Give the position of every Plasmodium parasite visible.
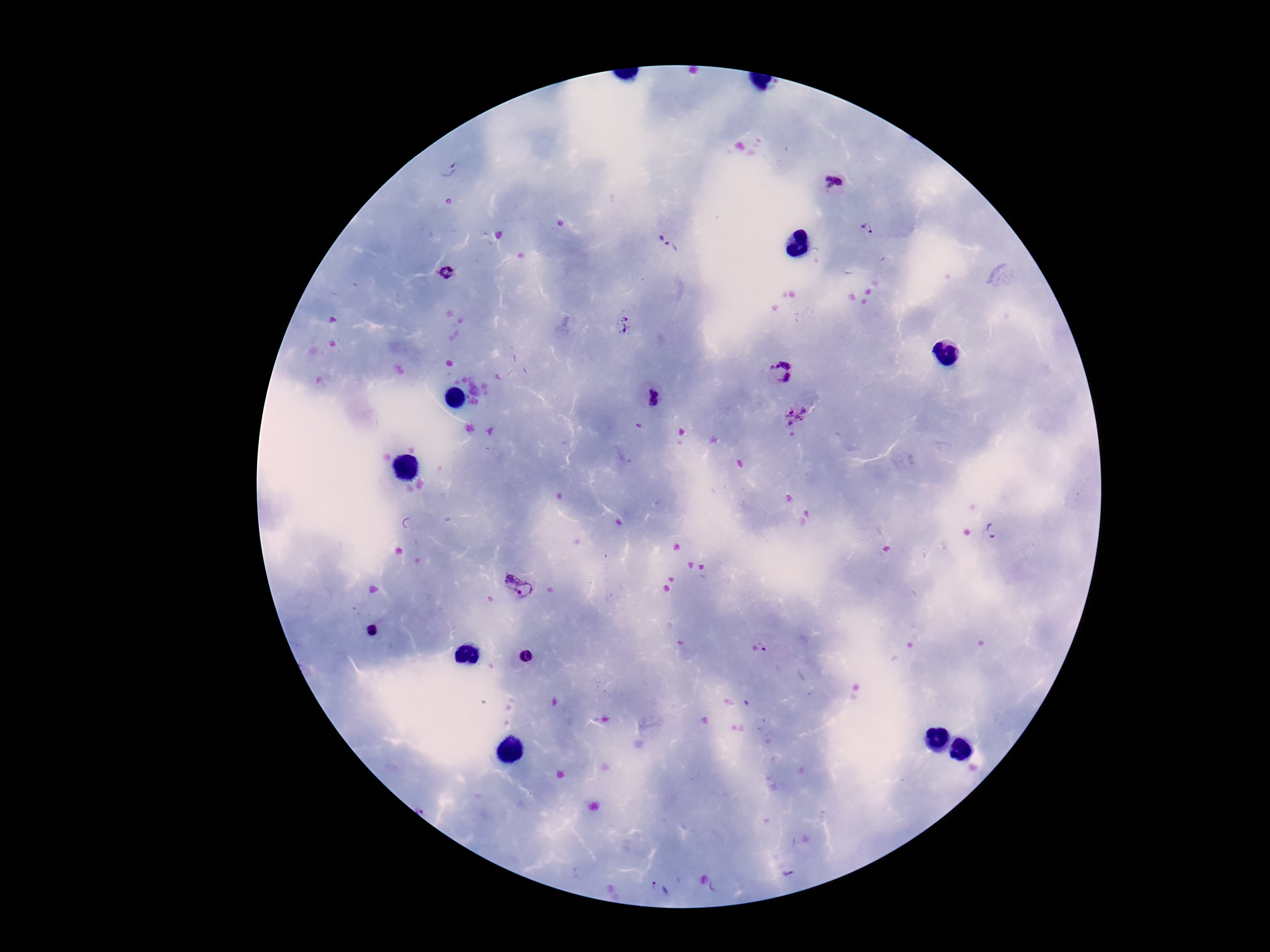
Approximate centers as {x, y} in pixels.
Plasmodium parasites: {447, 170}, {833, 180}, {869, 228}, {664, 238}, {449, 273}, {624, 324}, {782, 370}, {651, 399}, {795, 412}, {991, 531}, {519, 587}, {759, 648}, {658, 889}.

One field from this slide. Giemsa-stained preparation. Thick peripheral-blood smear. Patient malaria status: infected. Image is 1270×952 pixels. Photographed through the microscope eyepiece with a smartphone camera. 100x magnification.